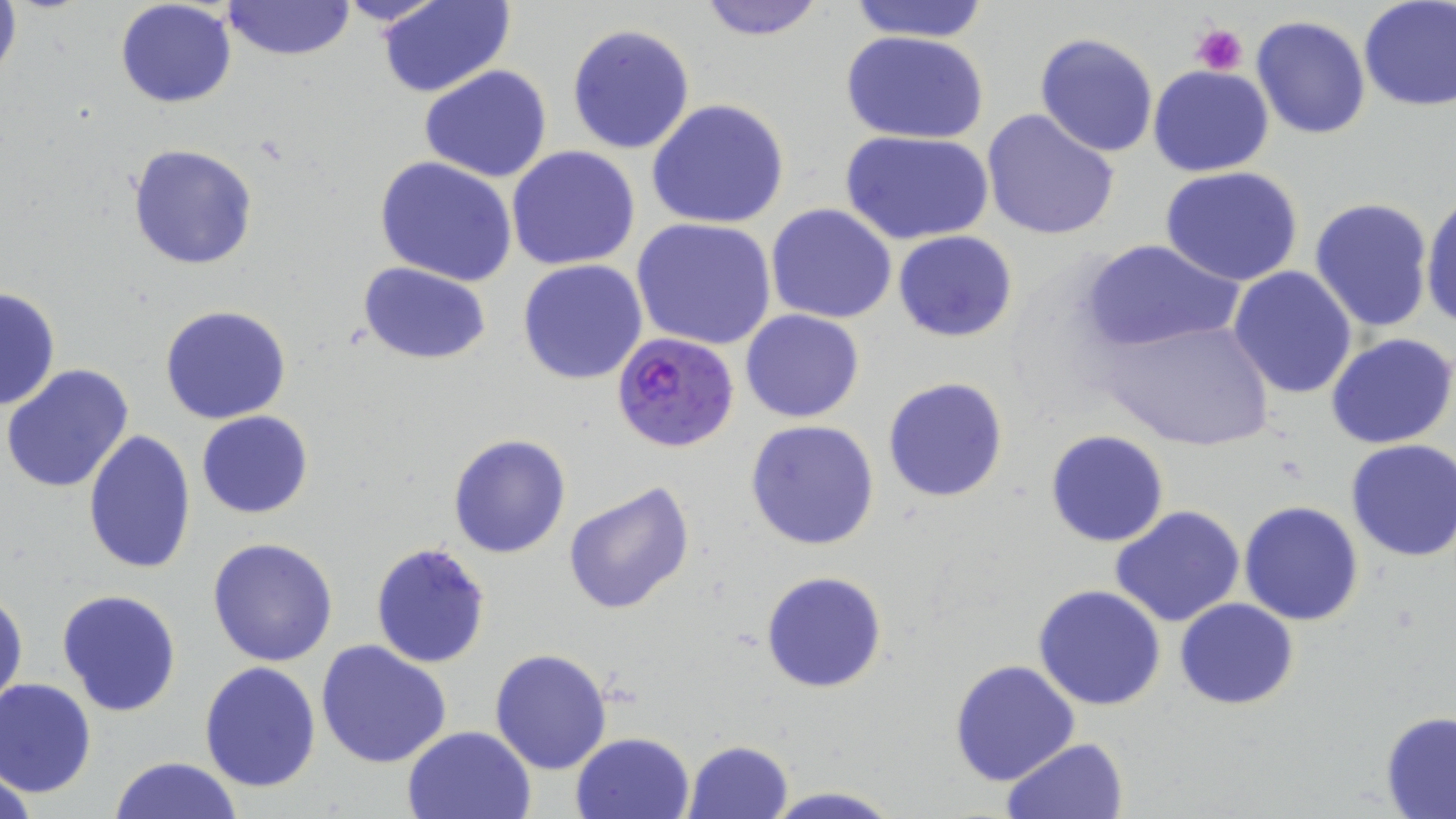
{
  "slide_level_diagnosis": "Plasmodium falciparum",
  "image_size": "1456×819 pixels",
  "preparation": "thin blood film",
  "platelet_locations": "approximate bounding boxes as (x1, y1, x2, y2) in pixels: (1192, 20, 1248, 77)",
  "stain": "May-Grünwald-Giemsa",
  "modality": "optical microscopy",
  "magnification": "1000x",
  "uninfected_red_blood_cell_locations": "approximate bounding boxes as (x1, y1, x2, y2) in pixels: (0, 0, 22, 89), (222, 0, 353, 60), (332, 0, 449, 28), (377, 0, 516, 98), (693, 0, 829, 42), (1358, 0, 1456, 111), (114, 1, 237, 108), (841, 1, 994, 44), (1250, 14, 1373, 139), (566, 23, 696, 156), (842, 29, 990, 145), (1034, 32, 1160, 157), (419, 64, 552, 184), (1149, 65, 1275, 178), (646, 98, 790, 230), (982, 109, 1121, 242), (844, 130, 995, 243), (127, 144, 257, 269), (507, 146, 641, 269), (374, 155, 518, 286), (1159, 166, 1305, 286), (1420, 192, 1456, 332), (1308, 197, 1435, 332), (766, 204, 897, 323), (633, 219, 777, 352), (893, 231, 1018, 342), (1079, 238, 1239, 354), (517, 259, 649, 385), (358, 263, 492, 364), (1228, 265, 1360, 398), (0, 287, 61, 412), (161, 305, 291, 424), (740, 309, 866, 424), (1097, 317, 1278, 454), (1326, 333, 1456, 449), (2, 365, 134, 495), (881, 376, 1009, 504), (196, 410, 313, 520), (745, 419, 880, 552), (1045, 430, 1168, 547), (82, 431, 197, 578), (447, 432, 571, 558), (1345, 438, 1456, 562), (563, 480, 695, 617), (1239, 500, 1364, 626), (1110, 506, 1245, 627), (208, 536, 339, 667), (370, 542, 490, 667), (761, 570, 888, 693), (1033, 585, 1166, 712), (57, 588, 183, 717), (1, 590, 27, 712), (1174, 598, 1298, 709), (315, 639, 452, 769), (489, 647, 613, 774), (949, 660, 1081, 785), (199, 662, 322, 793), (0, 678, 96, 797), (1380, 710, 1456, 817), (401, 724, 536, 818), (570, 732, 695, 819), (1001, 737, 1129, 818), (682, 740, 796, 819), (108, 756, 245, 818), (761, 786, 902, 819)",
  "field_of_view": "single",
  "plasmodium_falciparum_infected_red_blood_cell_locations": "approximate bounding boxes as (x1, y1, x2, y2) in pixels: (610, 333, 740, 453)"
}